Name the parasite shown.
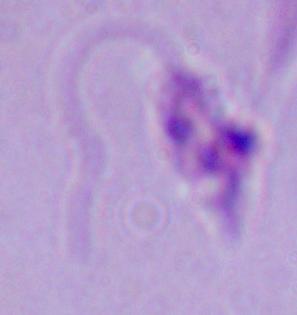
Leishmania.

Summary:
  - Magnification: 1000x
  - Modality: photomicrograph